Assess the morphology of the red blood cells.
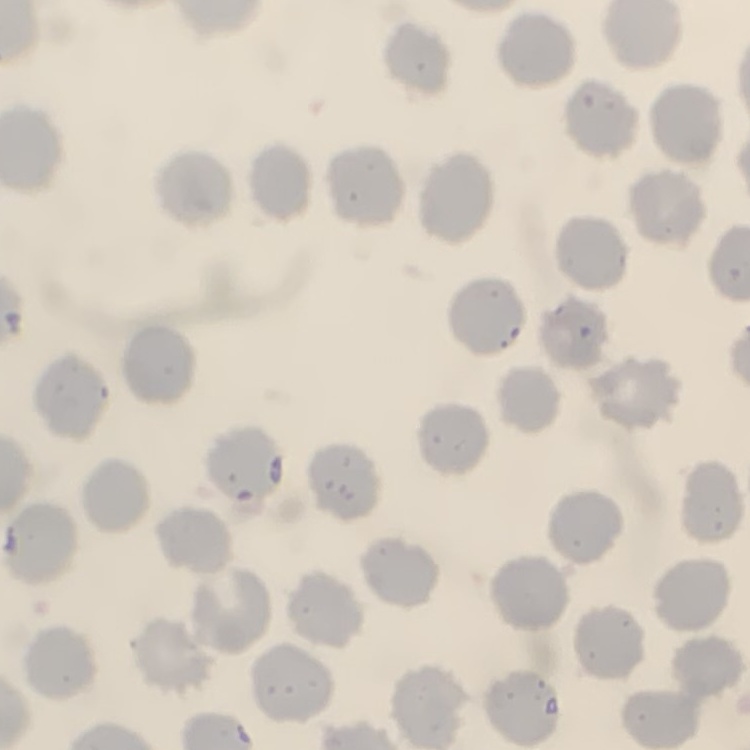

They show no rouleaux formation.

Summary:
  - Stain: Field's or Giemsa
  - Image type: square crop of a larger photomicrograph
  - Preparation: thin blood smear